Give the position of every Plasmodium parasite visible.
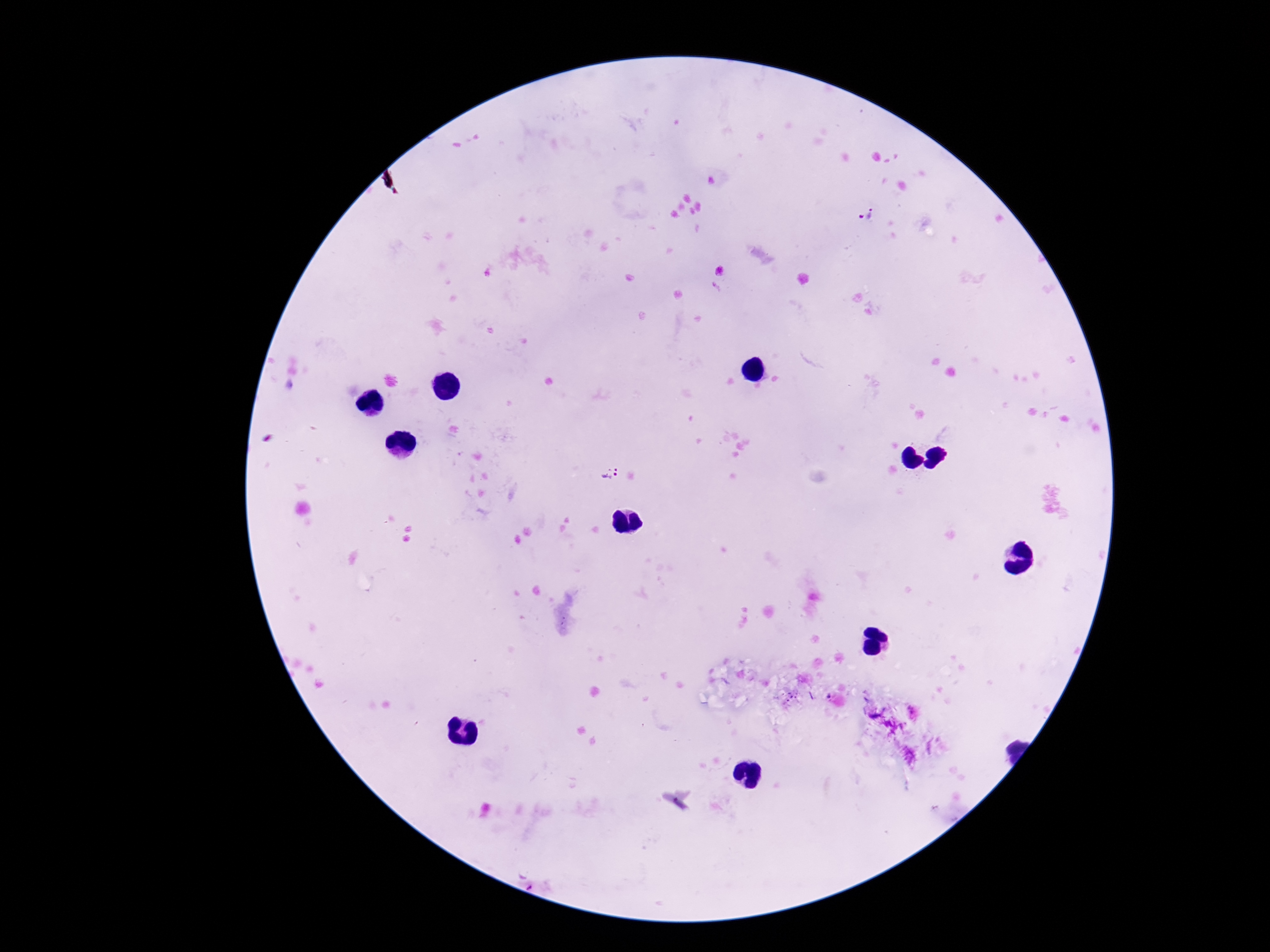
Approximate centers as (x, y) in pixels.
Plasmodium parasites: (868, 215), (608, 473).

One field from this slide. 100x magnification. Photographed through the microscope eyepiece with a smartphone camera. Image is 1270×952 pixels. Giemsa stain. Patient malaria status: positive. Thick blood film.